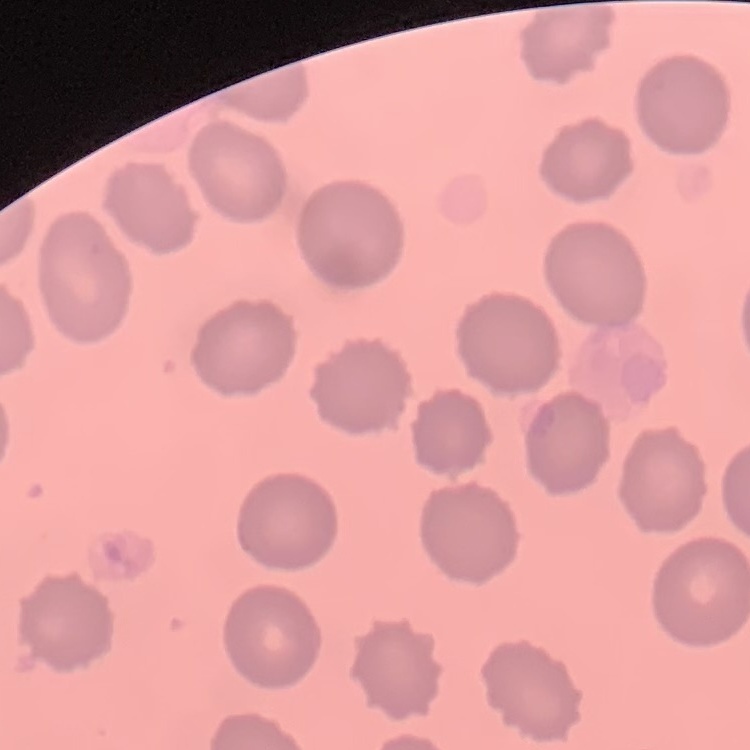
red blood cell morphology = no rouleaux formation
stain = Field's or Giemsa
preparation = thin blood smear
image type = one tile cut from a larger photomicrograph